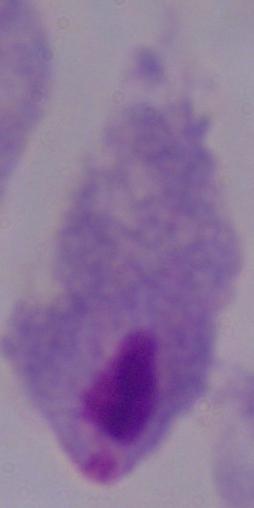
Captured at 1000x magnification. A trichomonad is seen. Micrograph.